Assess the morphology of the erythrocytes.
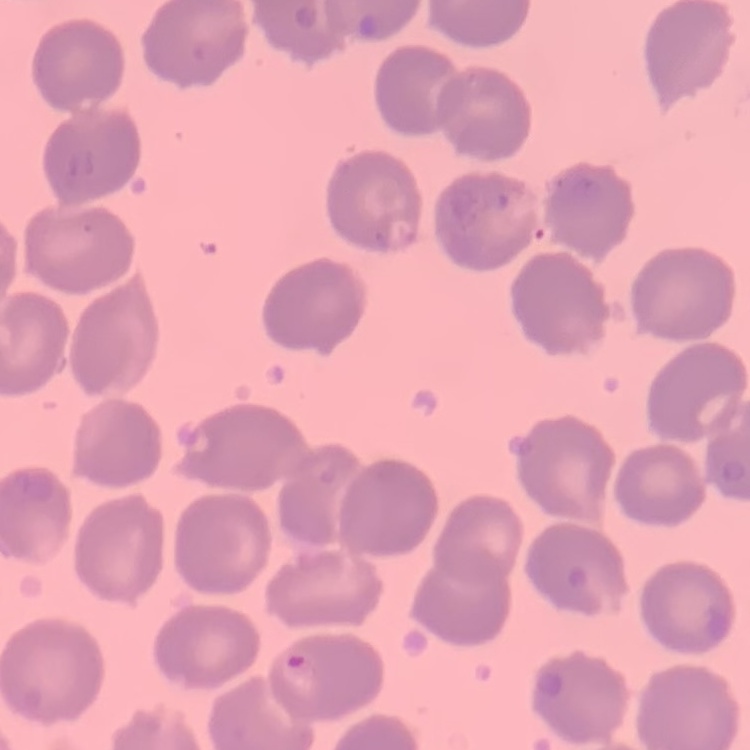

No rouleaux formation.

preparation = thin blood film
image type = square crop of a larger photomicrograph
stain = Field's or Giemsa